Give the extent of all Babesia divergens-infected red blood cells.
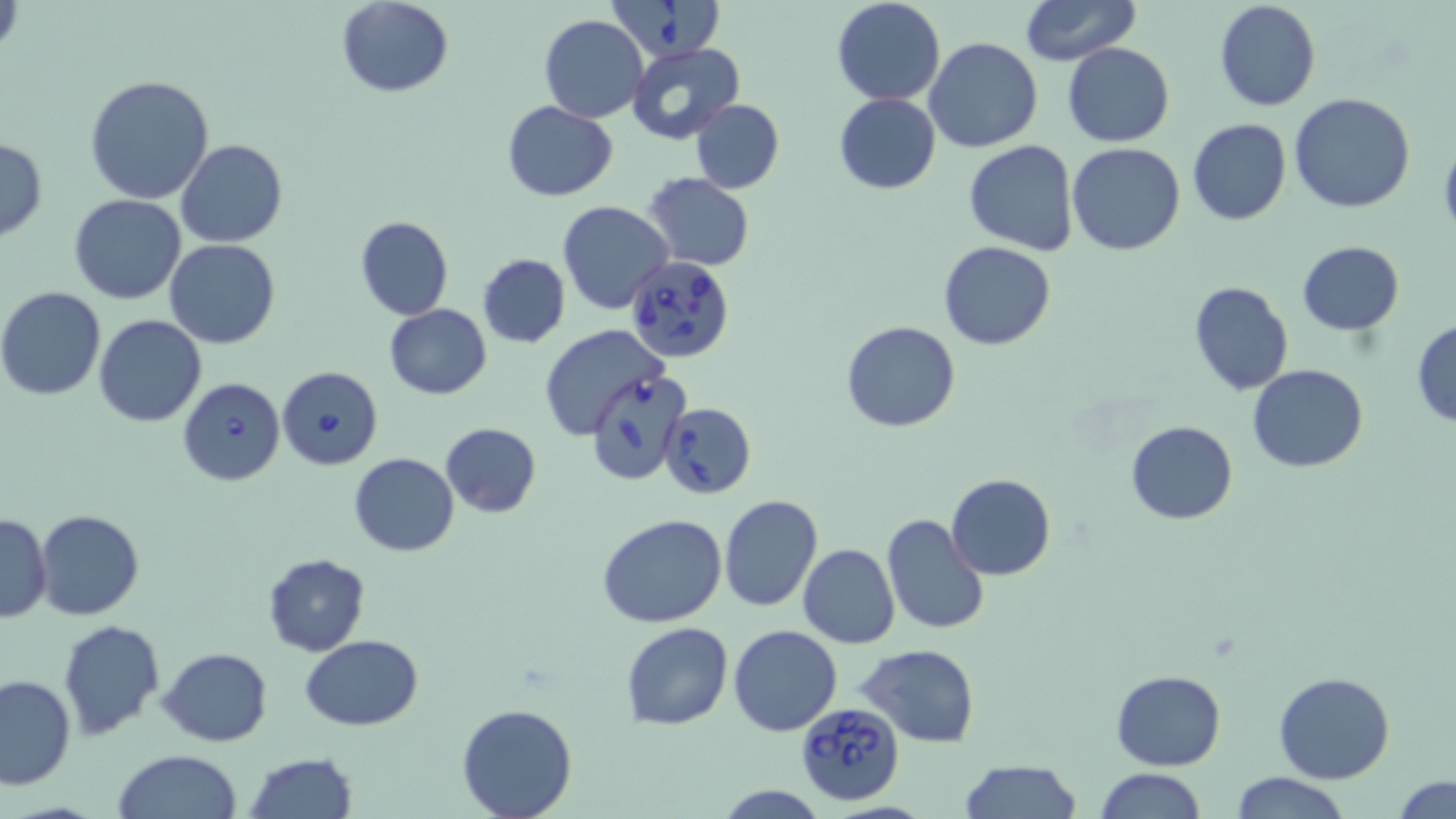

Approximate bounding boxes as (x1, y1, x2, y2) in pixels.
Babesia divergens-infected red blood cells: (607, 0, 726, 59), (626, 254, 735, 364), (279, 363, 385, 472), (586, 369, 692, 486), (178, 377, 285, 485), (660, 401, 755, 500), (794, 700, 904, 804).

Summary:
  - Uninfected red blood cell locations: (831, 0, 945, 106), (1019, 0, 1139, 65), (1213, 0, 1321, 112), (337, 1, 454, 97), (539, 15, 649, 123), (923, 38, 1042, 153), (626, 42, 744, 143), (1062, 43, 1176, 147), (83, 75, 215, 205), (833, 93, 941, 193), (1289, 93, 1416, 213), (689, 98, 784, 194), (502, 101, 618, 200), (1186, 118, 1292, 226), (0, 136, 47, 242), (175, 139, 288, 248), (964, 141, 1079, 256), (1066, 142, 1185, 255), (643, 173, 755, 270), (69, 195, 188, 305), (557, 201, 673, 315), (355, 216, 452, 321), (165, 239, 280, 349), (1297, 239, 1406, 337), (939, 241, 1055, 349), (477, 253, 570, 347), (1189, 282, 1294, 396), (0, 287, 106, 399), (1, 299, 208, 412), (384, 304, 491, 399), (93, 314, 207, 428), (1412, 318, 1456, 429), (843, 321, 961, 434), (541, 326, 667, 439), (1247, 364, 1368, 472), (1125, 420, 1239, 524), (439, 421, 543, 517), (350, 453, 460, 556), (946, 473, 1057, 580), (718, 495, 823, 612), (35, 509, 143, 620), (880, 512, 990, 638), (0, 513, 51, 622), (598, 514, 728, 627), (798, 543, 900, 650), (262, 553, 369, 655), (57, 618, 166, 740), (620, 622, 734, 730), (729, 624, 842, 737), (300, 634, 423, 731), (858, 645, 981, 746), (158, 648, 272, 745), (1112, 668, 1224, 769), (1272, 672, 1396, 785), (0, 674, 75, 789), (457, 702, 577, 818), (112, 750, 244, 819), (244, 753, 359, 818), (958, 759, 1081, 818), (1094, 768, 1206, 819), (1226, 771, 1354, 818), (1393, 776, 1455, 817), (715, 785, 827, 818)
  - Slide-level diagnosis: Babesia divergens
  - Magnification: 1000x
  - Image size: 1456×819 pixels
  - Preparation: thin blood film
  - Stain: May-Grünwald-Giemsa
  - Modality: light microscopy
  - Field of view: single